Give the extent of all Plasmodium ovale-infected red blood cells.
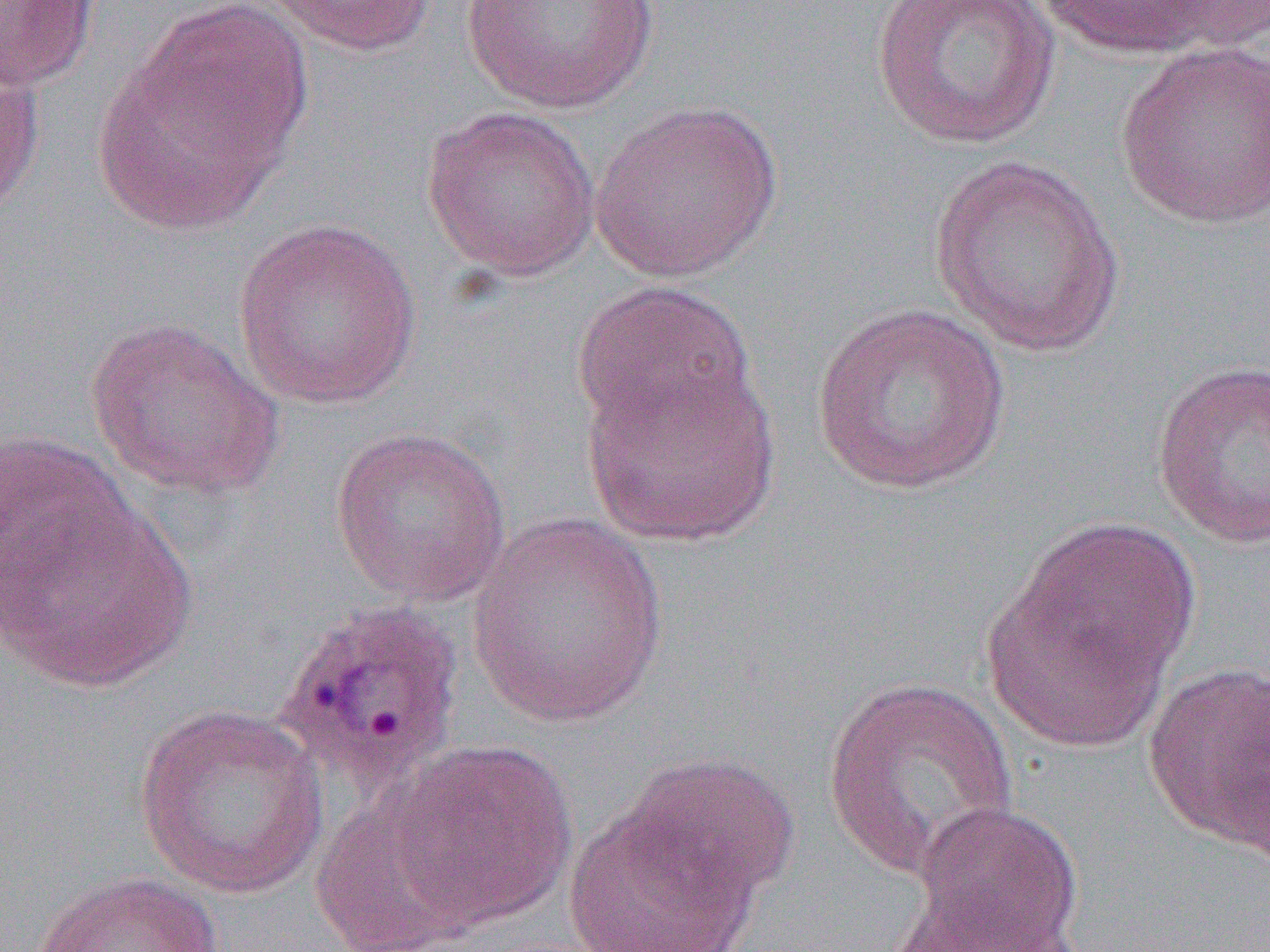
Approximate bounding boxes as [x1, y1, x2, y2] in pixels.
Plasmodium ovale-infected red blood cells: [271, 598, 467, 798].

slide-level diagnosis = Plasmodium ovale
magnification = 1000x
field of view = one of a larger specimen
preparation = thin blood smear
modality = optical microscopy
uninfected red blood cell locations = approximate bounding boxes as [x1, y1, x2, y2] in pixels: [0, 0, 100, 92], [260, 0, 440, 57], [459, 0, 660, 114], [869, 0, 1061, 150], [1035, 0, 1253, 63], [92, 18, 306, 239], [1114, 40, 1270, 231], [0, 44, 46, 218], [589, 99, 784, 283], [420, 105, 601, 282], [929, 154, 1126, 358], [232, 216, 424, 410], [571, 281, 757, 441], [810, 302, 1013, 497], [83, 316, 284, 499], [581, 353, 780, 548], [1151, 359, 1270, 549], [329, 426, 511, 607], [0, 428, 139, 622], [2, 487, 197, 695], [465, 515, 669, 727], [983, 521, 1197, 752], [1142, 663, 1269, 849], [821, 675, 1021, 882], [133, 705, 329, 899], [383, 737, 578, 931], [620, 752, 802, 908], [310, 797, 478, 952], [907, 799, 1085, 951], [561, 801, 763, 952], [31, 870, 225, 952], [882, 884, 1090, 951]
image size = 1270×952 pixels